Identify the blood parasite species.
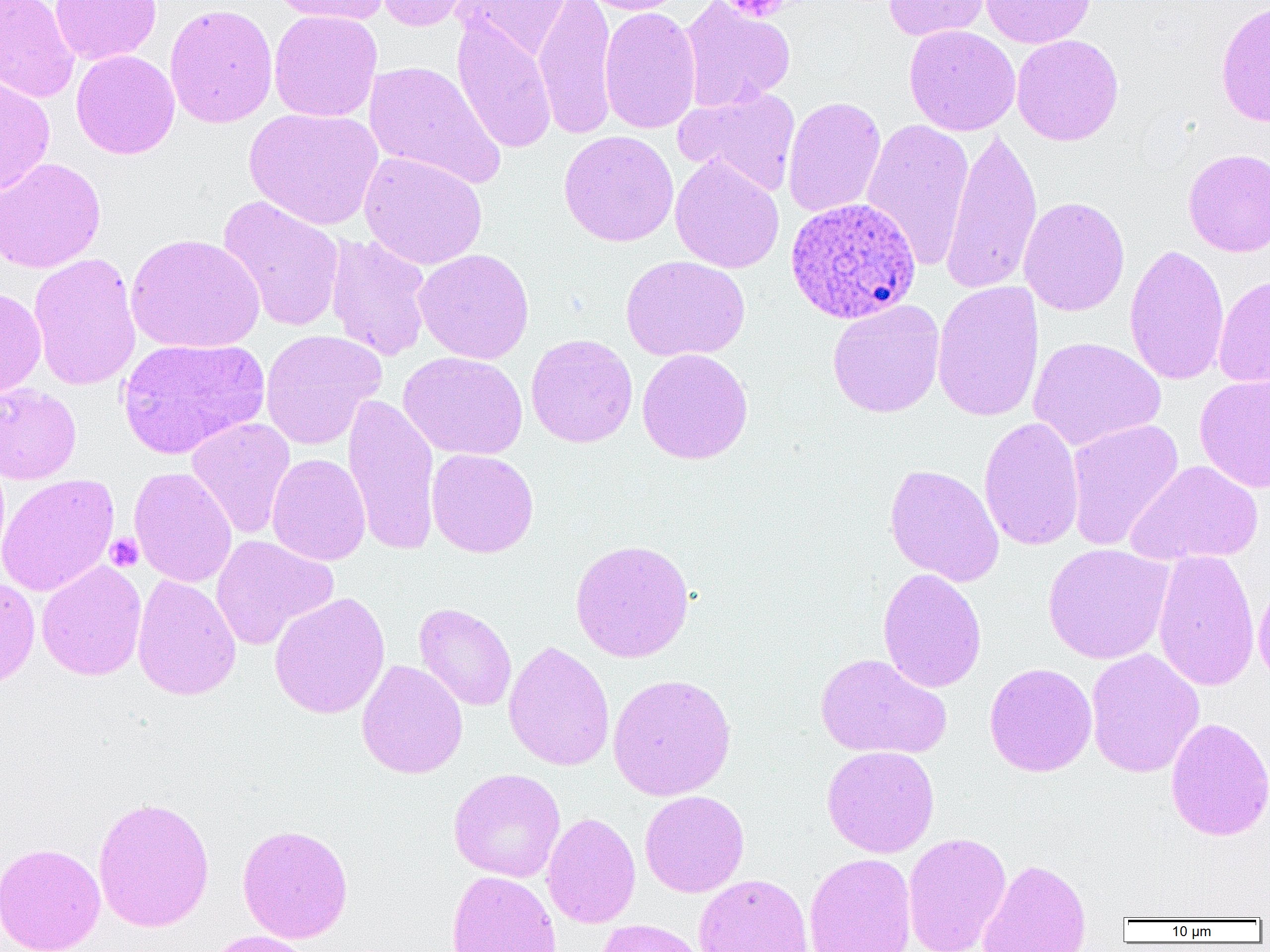
Plasmodium ovale.

Summary:
  - Coordinate format: approximate bounding boxes as (x1,y1)-(x2,y2) corner pairs in pixels
  - Plasmodium ovale-infected red blood cell locations: (780,198)-(916,325)
  - Uninfected red blood cell locations: (0,0)-(79,103), (50,0)-(162,65), (270,0)-(388,25), (373,0)-(480,33), (454,0)-(573,61), (533,0)-(619,140), (580,0)-(686,15), (882,0)-(992,42), (980,0)-(1094,48), (678,1)-(795,112), (1215,1)-(1270,129), (164,2)-(278,129), (599,6)-(701,134), (268,10)-(382,122), (451,15)-(557,154), (904,25)-(1020,136), (1011,34)-(1124,146), (71,50)-(180,159), (364,60)-(506,188), (0,75)-(55,196), (674,86)-(801,196), (782,95)-(886,218), (244,107)-(383,230), (861,118)-(976,271), (940,125)-(1042,296), (558,130)-(679,247), (1183,148)-(1270,257), (359,151)-(488,270), (670,154)-(785,274), (0,158)-(106,273), (217,195)-(346,333), (1018,196)-(1130,317), (126,233)-(265,354), (325,233)-(433,362), (1124,244)-(1229,386), (414,248)-(535,365), (28,252)-(142,392), (621,255)-(750,362), (1212,275)-(1270,389), (931,281)-(1044,423), (0,287)-(47,400), (829,295)-(948,413), (260,329)-(386,450), (525,333)-(638,448), (1027,336)-(1166,451), (118,337)-(269,459), (637,348)-(754,465), (398,351)-(528,460), (1194,372)-(1270,494), (0,383)-(82,484), (342,392)-(441,556), (978,416)-(1084,551), (185,417)-(296,539), (1065,418)-(1184,551), (427,448)-(539,558), (266,453)-(371,566), (1126,460)-(1264,566), (884,463)-(1005,587), (129,467)-(237,587), (0,473)-(119,596), (210,535)-(338,651), (570,538)-(695,663), (1042,543)-(1174,665), (1152,549)-(1260,693), (36,560)-(147,681), (877,567)-(987,693), (1253,573)-(1270,693), (132,574)-(241,701), (0,576)-(41,691), (269,592)-(391,719), (414,602)-(517,712), (503,640)-(615,771), (1085,648)-(1204,778), (815,652)-(951,759), (356,659)-(468,779), (983,662)-(1097,777), (607,672)-(736,801), (1165,716)-(1270,842), (821,745)-(940,858), (448,768)-(566,882), (639,790)-(749,897), (93,795)-(215,933), (542,812)-(641,929), (237,823)-(354,944), (902,831)-(1011,952), (0,841)-(106,952), (803,852)-(917,952), (977,858)-(1091,952), (446,870)-(562,952), (694,873)-(813,952), (596,918)-(710,952), (203,930)-(316,952)
  - Platelet locations: (718,0)-(792,22), (105,533)-(143,572)
  - Magnification: 1000x
  - Field of view: single
  - Modality: optical microscopy
  - Image size: 1270×952 pixels
  - Preparation: thin blood film